Assess this cell for malaria.
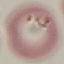

It is parasitized.

Thin smear of blood. Cell patch, automatically extracted from a larger field of view and resized to 64 × 64 pixels. Giemsa-stained preparation. Photographed with a smartphone camera at the microscope eyepiece.